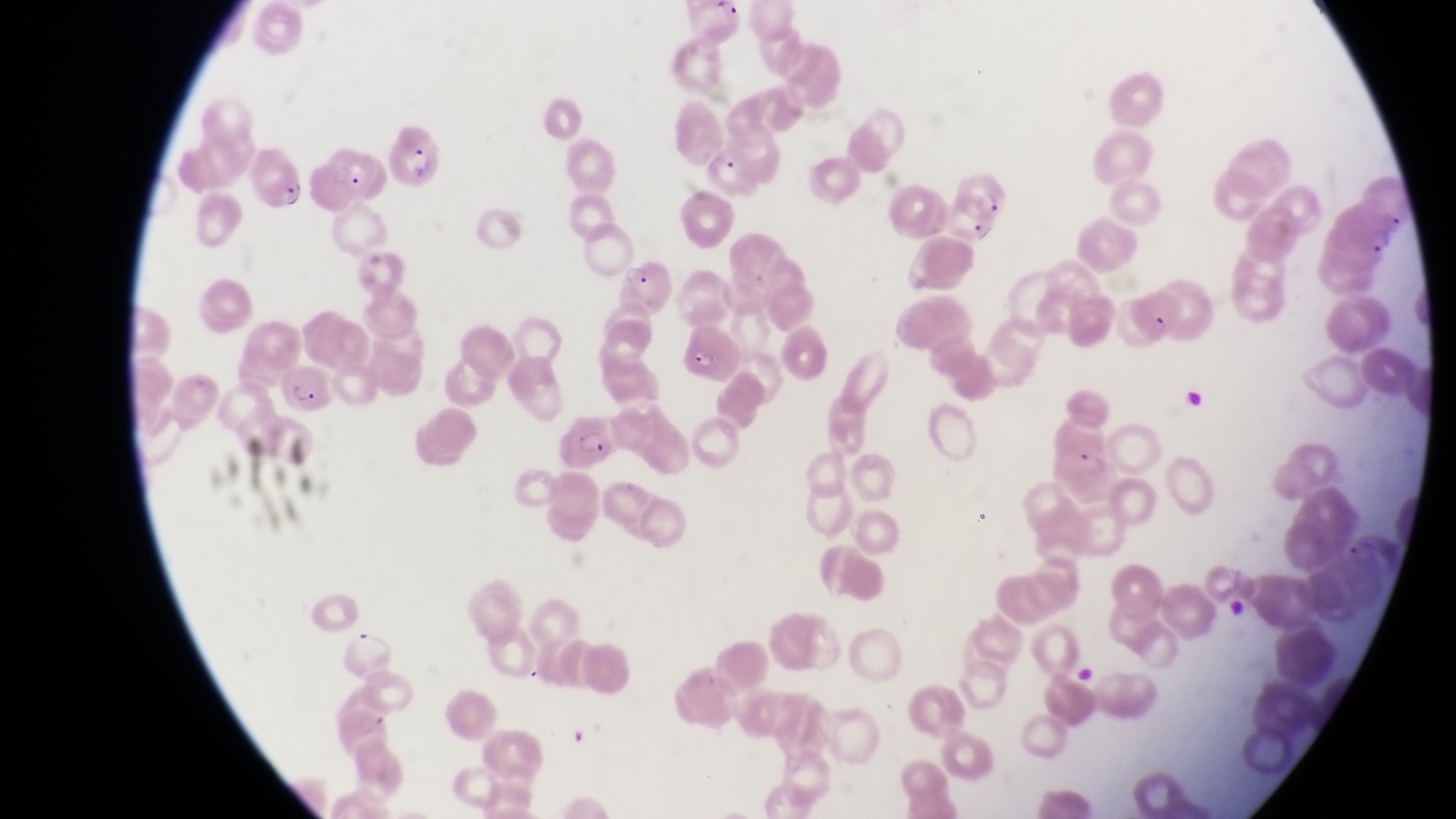

Approximate bounding boxes as (left, top, right, bottom) in pixels. Parasitised red blood cell locations: (391, 124, 441, 190), (706, 138, 762, 201), (320, 143, 393, 202), (254, 151, 306, 218), (951, 168, 1011, 227), (620, 261, 672, 314), (1131, 285, 1183, 343), (682, 327, 746, 382), (285, 362, 334, 414), (563, 415, 622, 473), (1344, 528, 1387, 575). One field of view. Image is 1456×819 pixels. Captured by a smartphone held over the eyepiece of an Olympus CX-23 microscope. Magnification of 1000x. Collected in Uganda. Thin blood film.